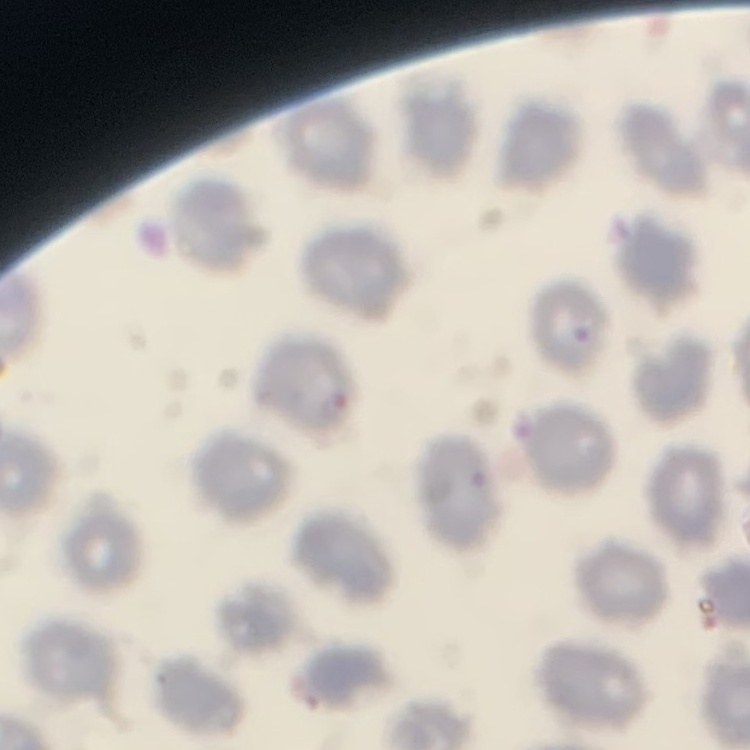

The erythrocytes show no rouleaux formation. Thin blood smear. One tile cut from a larger photomicrograph. Stained with either Field's or Giemsa.